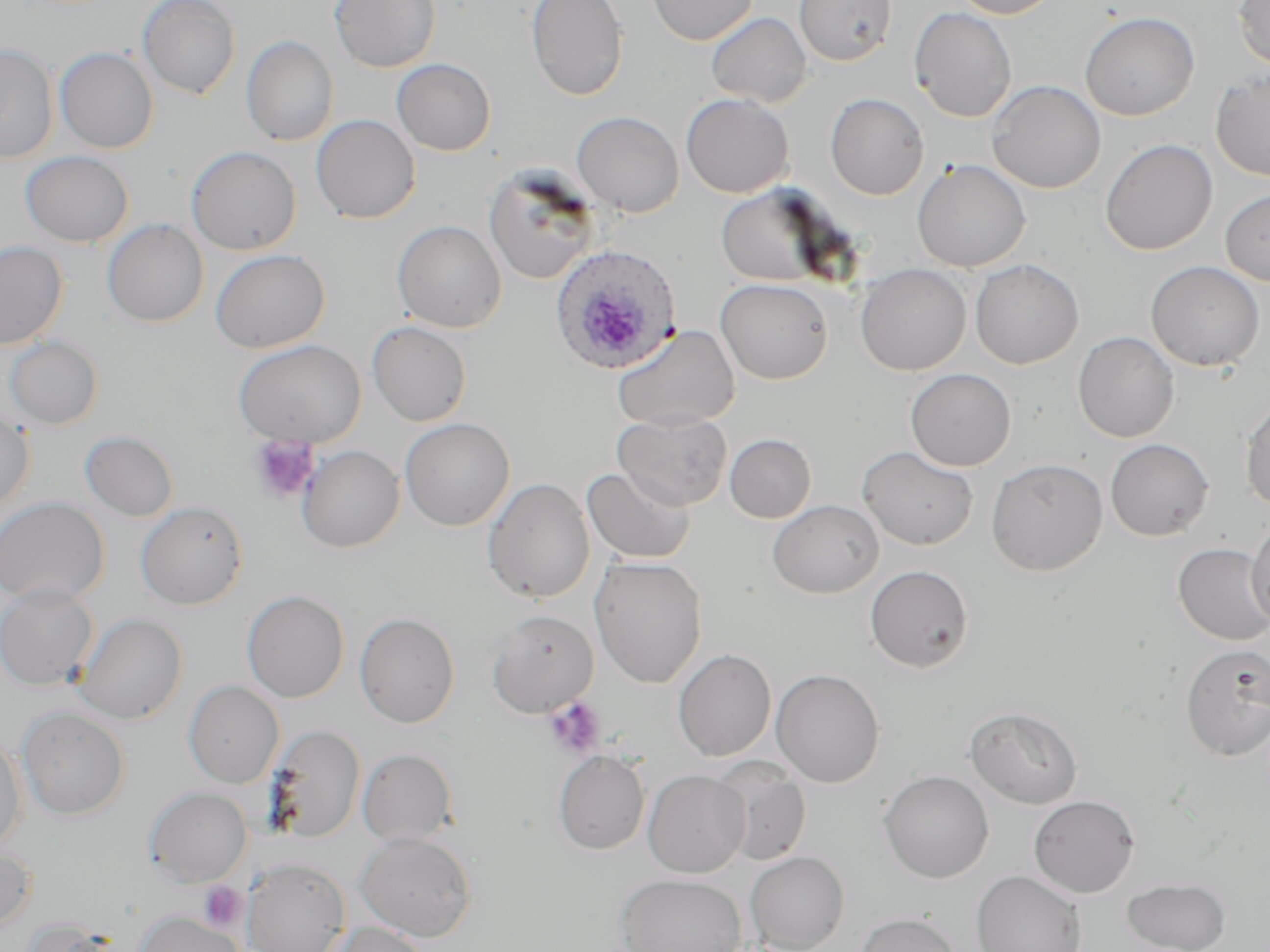

slide-level diagnosis = Plasmodium ovale
magnification = 1000x
platelet locations = approximate bounding boxes as [x1, y1, x2, y2] in pixels: [248, 435, 319, 503], [543, 696, 606, 758], [198, 882, 248, 931]
modality = light microscopy
Plasmodium ovale-infected red blood cell locations = approximate bounding boxes as [x1, y1, x2, y2] in pixels: [549, 243, 681, 375]
preparation = thin blood smear
stain = May-Grünwald-Giemsa
image size = 1270×952 pixels
uninfected red blood cell locations = approximate bounding boxes as [x1, y1, x2, y2] in pixels: [137, 0, 241, 100], [329, 0, 441, 73], [525, 0, 629, 101], [647, 0, 757, 45], [793, 0, 897, 65], [949, 0, 1062, 18], [1233, 0, 1270, 69], [909, 7, 1018, 122], [1079, 11, 1199, 120], [706, 12, 813, 108], [241, 36, 339, 147], [0, 42, 59, 164], [55, 47, 159, 154], [391, 58, 496, 156], [1210, 68, 1270, 181], [987, 80, 1106, 193], [681, 93, 794, 198], [825, 93, 930, 200], [571, 111, 684, 217], [310, 115, 420, 224], [1099, 138, 1218, 255], [186, 146, 301, 255], [20, 151, 134, 247], [912, 159, 1031, 272], [483, 166, 600, 285], [715, 186, 834, 287], [1220, 188, 1270, 286], [102, 219, 209, 327], [392, 220, 507, 333], [0, 240, 68, 349], [210, 249, 330, 353], [970, 259, 1084, 369], [1146, 261, 1265, 371], [855, 264, 972, 375], [715, 278, 834, 384], [367, 321, 472, 426], [612, 324, 740, 430], [1073, 331, 1179, 442], [3, 336, 104, 430], [233, 339, 365, 447], [905, 368, 1016, 471], [1240, 398, 1270, 513], [0, 408, 35, 515], [613, 410, 733, 510], [399, 417, 515, 531], [80, 430, 179, 521], [725, 433, 816, 522], [1105, 439, 1214, 541], [296, 445, 405, 552], [857, 445, 978, 550], [986, 458, 1107, 575], [581, 466, 696, 564], [482, 478, 595, 604], [0, 497, 109, 606], [767, 500, 884, 598], [135, 502, 248, 610], [1246, 518, 1270, 631], [1172, 543, 1270, 645], [589, 556, 708, 688], [865, 565, 973, 671], [0, 582, 99, 691], [242, 590, 349, 703], [485, 609, 598, 718], [355, 612, 460, 728], [75, 613, 188, 724], [1180, 644, 1270, 761], [673, 648, 776, 761], [770, 668, 885, 787], [183, 680, 284, 788], [17, 706, 130, 820], [965, 706, 1083, 809], [263, 724, 366, 843], [0, 734, 27, 852], [357, 748, 458, 846], [554, 751, 650, 854], [711, 759, 812, 866], [643, 769, 750, 878], [878, 770, 994, 883], [144, 786, 252, 887], [1028, 795, 1139, 897], [354, 831, 476, 942], [0, 841, 37, 931], [744, 851, 850, 952], [241, 858, 350, 952], [971, 871, 1087, 952], [615, 873, 747, 952], [1123, 878, 1231, 952], [134, 910, 243, 952], [855, 911, 962, 952], [18, 918, 119, 952], [322, 922, 431, 952]
field of view = one of a larger specimen